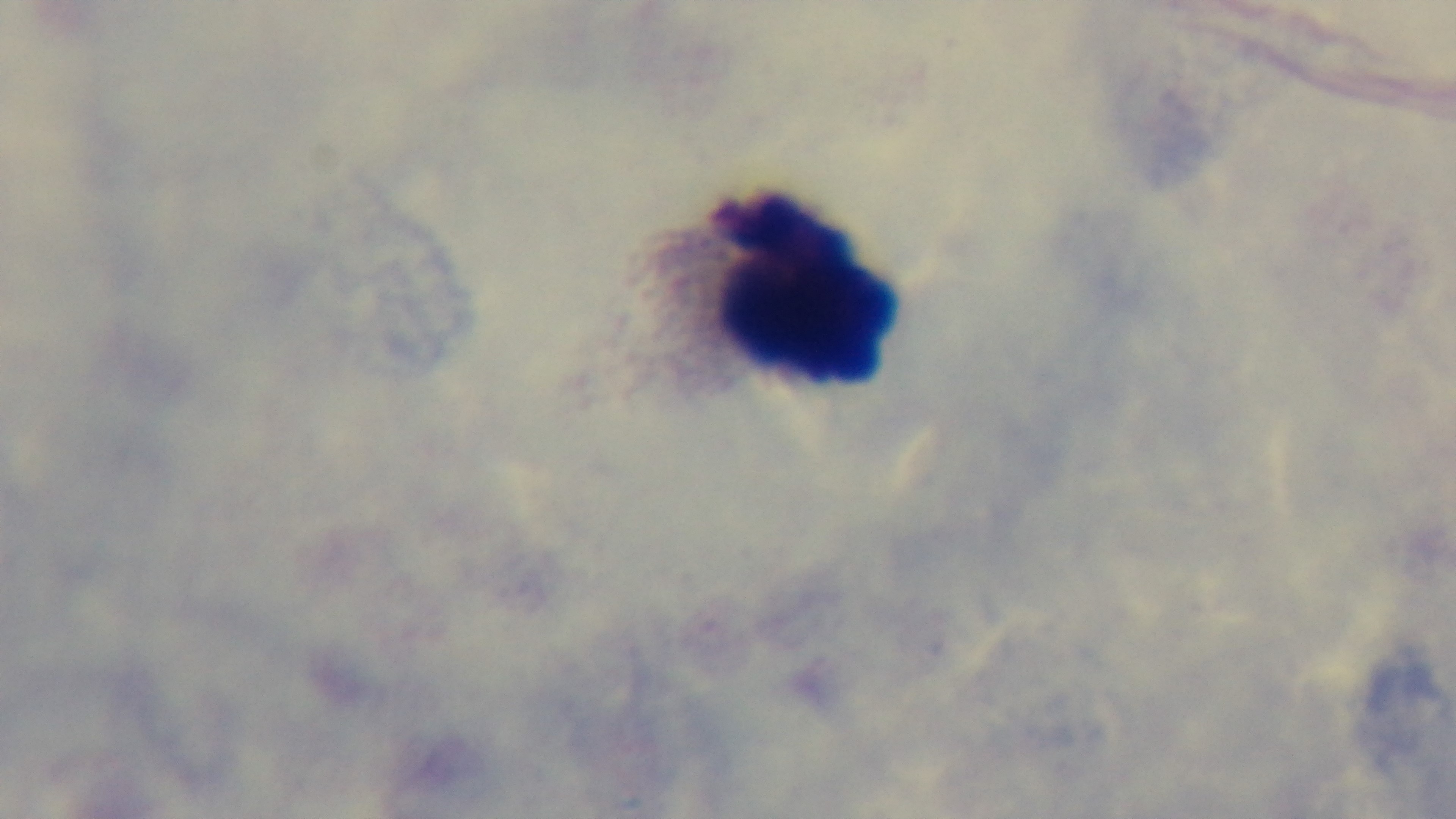
objective = 100x oil immersion
malaria status = negative
preparation = thick blood film
field of view = single
stain = Giemsa
capture = mounted 4K digital camera
modality = light microscopy